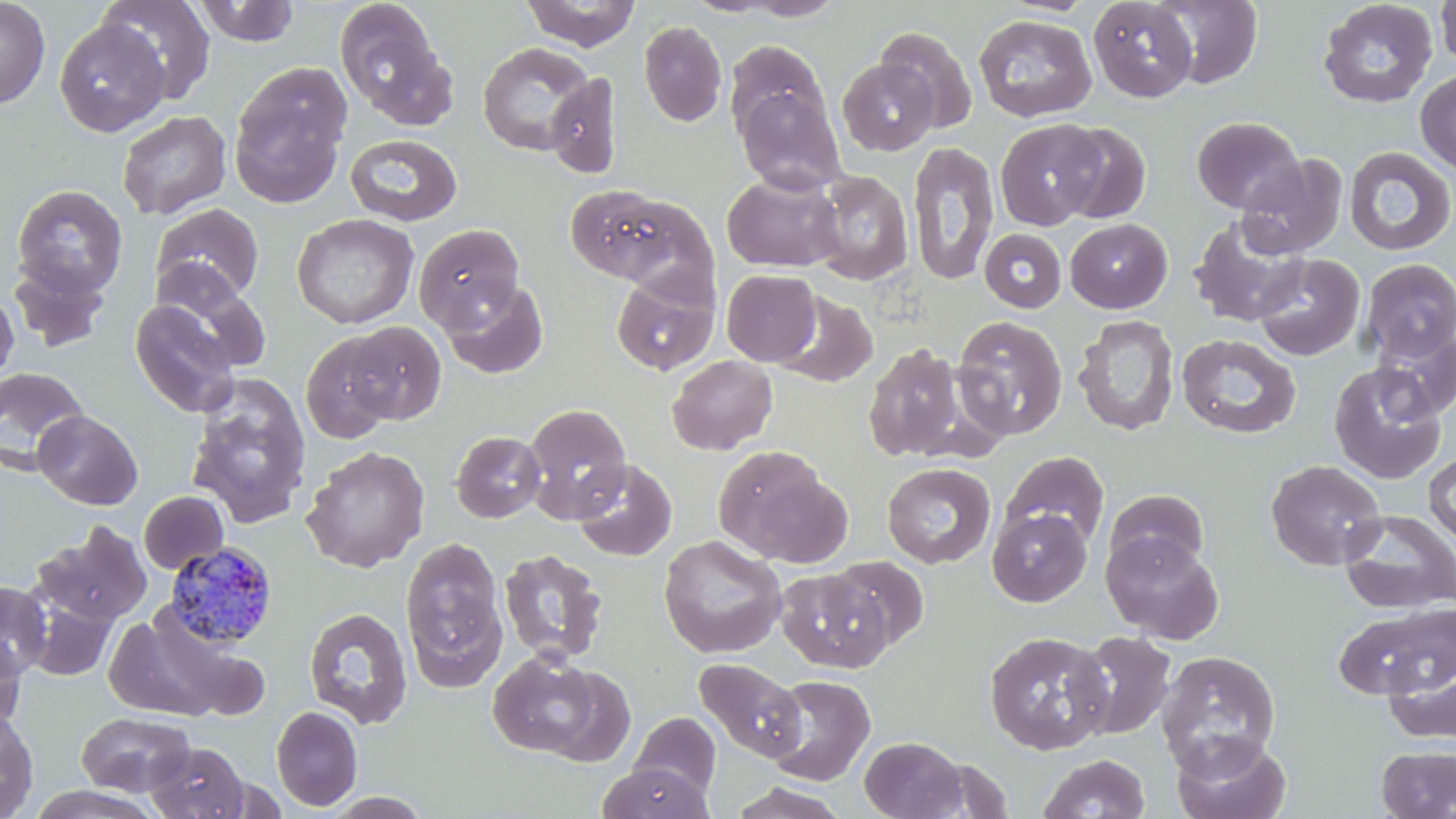

slide_level_diagnosis: Plasmodium malariae
preparation: thin blood smear
uninfected_red_blood_cell_locations: 'approximate bounding boxes as [x1, y1, x2, y2] in pixels: [0, 0, 51, 108], [99, 0, 217, 105], [519, 0, 641, 50], [730, 0, 850, 21], [1088, 0, 1198, 102], [1151, 0, 1264, 89], [192, 1, 301, 46], [1317, 1, 1438, 109], [1435, 1, 1456, 71], [334, 2, 451, 125], [973, 14, 1097, 122], [53, 17, 170, 137], [638, 21, 727, 126], [875, 26, 978, 133], [724, 40, 830, 144], [477, 42, 593, 156], [838, 58, 937, 155], [229, 63, 352, 207], [1415, 68, 1456, 176], [544, 72, 623, 177], [734, 84, 846, 194], [117, 110, 232, 220], [1191, 116, 1305, 214], [995, 118, 1104, 230], [1054, 122, 1152, 224], [345, 134, 463, 226], [908, 140, 999, 287], [1343, 145, 1456, 256], [1237, 153, 1348, 259], [809, 170, 913, 286], [721, 172, 843, 272], [12, 185, 127, 299], [563, 185, 690, 287], [151, 203, 264, 304], [292, 213, 418, 329], [1189, 217, 1310, 327], [1065, 218, 1172, 313], [414, 223, 524, 331], [980, 228, 1067, 313], [1253, 253, 1364, 361], [8, 258, 114, 351], [1360, 258, 1456, 362], [721, 269, 821, 366], [154, 271, 271, 374], [610, 271, 720, 376], [441, 277, 548, 378], [0, 289, 19, 387], [773, 291, 878, 388], [129, 297, 242, 418], [951, 314, 1068, 440], [1073, 315, 1179, 436], [341, 321, 446, 426], [1371, 328, 1456, 419], [301, 333, 398, 444], [1176, 333, 1301, 439], [862, 342, 966, 463], [667, 355, 777, 455], [1329, 361, 1447, 483], [0, 367, 89, 471], [186, 376, 312, 530], [522, 403, 632, 522], [34, 410, 143, 510], [451, 431, 546, 522], [301, 445, 430, 573], [713, 447, 841, 563], [1000, 450, 1110, 549], [1424, 453, 1456, 546], [571, 458, 677, 561], [1265, 460, 1386, 571], [882, 462, 996, 568], [1104, 489, 1209, 575], [139, 491, 228, 574], [987, 508, 1092, 606], [1339, 510, 1456, 614], [32, 522, 152, 627], [1101, 531, 1223, 643], [658, 534, 787, 658], [399, 535, 508, 692], [499, 548, 608, 666], [829, 556, 929, 651], [773, 567, 884, 786], [776, 568, 892, 673], [0, 581, 51, 681], [20, 586, 119, 682], [1333, 600, 1454, 701], [303, 607, 413, 729], [102, 610, 249, 722], [984, 630, 1113, 755], [1070, 630, 1178, 739], [0, 638, 26, 734], [488, 651, 602, 758], [1156, 651, 1281, 775], [1382, 651, 1456, 744], [694, 658, 806, 763], [539, 667, 638, 766], [762, 674, 876, 786], [271, 706, 363, 811], [0, 711, 38, 819], [77, 711, 195, 796], [630, 712, 721, 801], [1171, 732, 1291, 819], [859, 735, 967, 818], [146, 741, 251, 819], [1375, 745, 1456, 818], [1038, 753, 1150, 818], [597, 762, 711, 819], [727, 781, 853, 819]'
stain: May-Grünwald-Giemsa
modality: light microscopy
plasmodium_malariae_infected_red_blood_cell_locations: 'approximate bounding boxes as [x1, y1, x2, y2] in pixels: [165, 542, 279, 650]'
magnification: 1000x
field_of_view: single
image_size: 1456×819 pixels